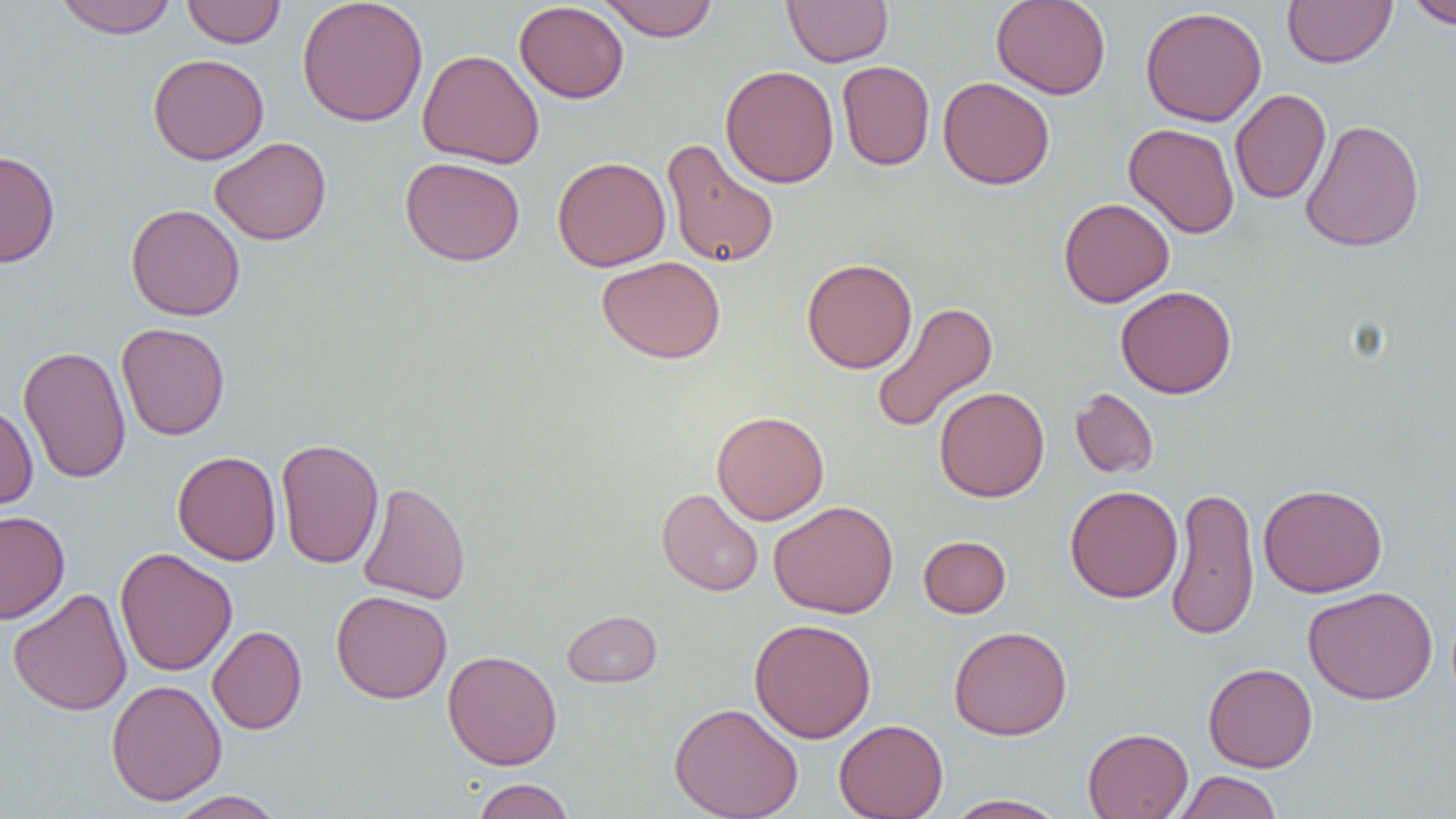
Approximate bounding boxes as [x1, y1, x2, y2] in pixels. Uninfected red blood cell locations: [52, 0, 179, 38], [181, 0, 286, 48], [599, 0, 719, 42], [783, 0, 893, 66], [991, 0, 1111, 99], [1282, 0, 1397, 68], [1405, 0, 1456, 29], [297, 1, 428, 127], [514, 1, 629, 103], [1140, 6, 1267, 126], [416, 49, 545, 168], [148, 53, 269, 165], [837, 61, 935, 171], [720, 64, 839, 188], [938, 77, 1056, 189], [1230, 89, 1331, 204], [1299, 118, 1425, 253], [1124, 122, 1240, 238], [209, 137, 331, 245], [661, 138, 779, 268], [0, 149, 60, 268], [400, 156, 525, 266], [552, 156, 671, 271], [1058, 197, 1174, 307], [125, 204, 245, 321], [596, 256, 726, 363], [802, 258, 917, 374], [1115, 285, 1237, 399], [870, 301, 998, 435], [116, 322, 230, 441], [18, 345, 131, 484], [934, 386, 1050, 502], [1070, 388, 1159, 479], [0, 402, 38, 512], [711, 410, 828, 525], [276, 438, 384, 569], [172, 450, 282, 566], [357, 481, 471, 605], [1258, 483, 1388, 598], [1065, 485, 1182, 603], [1165, 485, 1260, 641], [656, 488, 763, 597], [769, 501, 898, 618], [0, 509, 70, 624], [918, 535, 1011, 618], [114, 547, 237, 677], [1303, 585, 1438, 704], [7, 587, 132, 716], [331, 590, 452, 703], [562, 610, 662, 688], [749, 618, 877, 743], [208, 625, 307, 734], [948, 625, 1072, 740], [442, 650, 562, 770], [1203, 662, 1318, 772], [106, 679, 227, 805], [669, 702, 803, 819], [834, 718, 948, 819], [1082, 727, 1193, 819], [1174, 770, 1283, 819], [470, 778, 575, 818], [167, 790, 286, 819], [943, 793, 1070, 819]. Slide-level diagnosis: no evidence of blood parasites. Captured at 1000x magnification. Light microscopy. One field of a larger specimen. Thin blood smear. Image is 1456×819 pixels.